Locate every leukocyte (white blood cell).
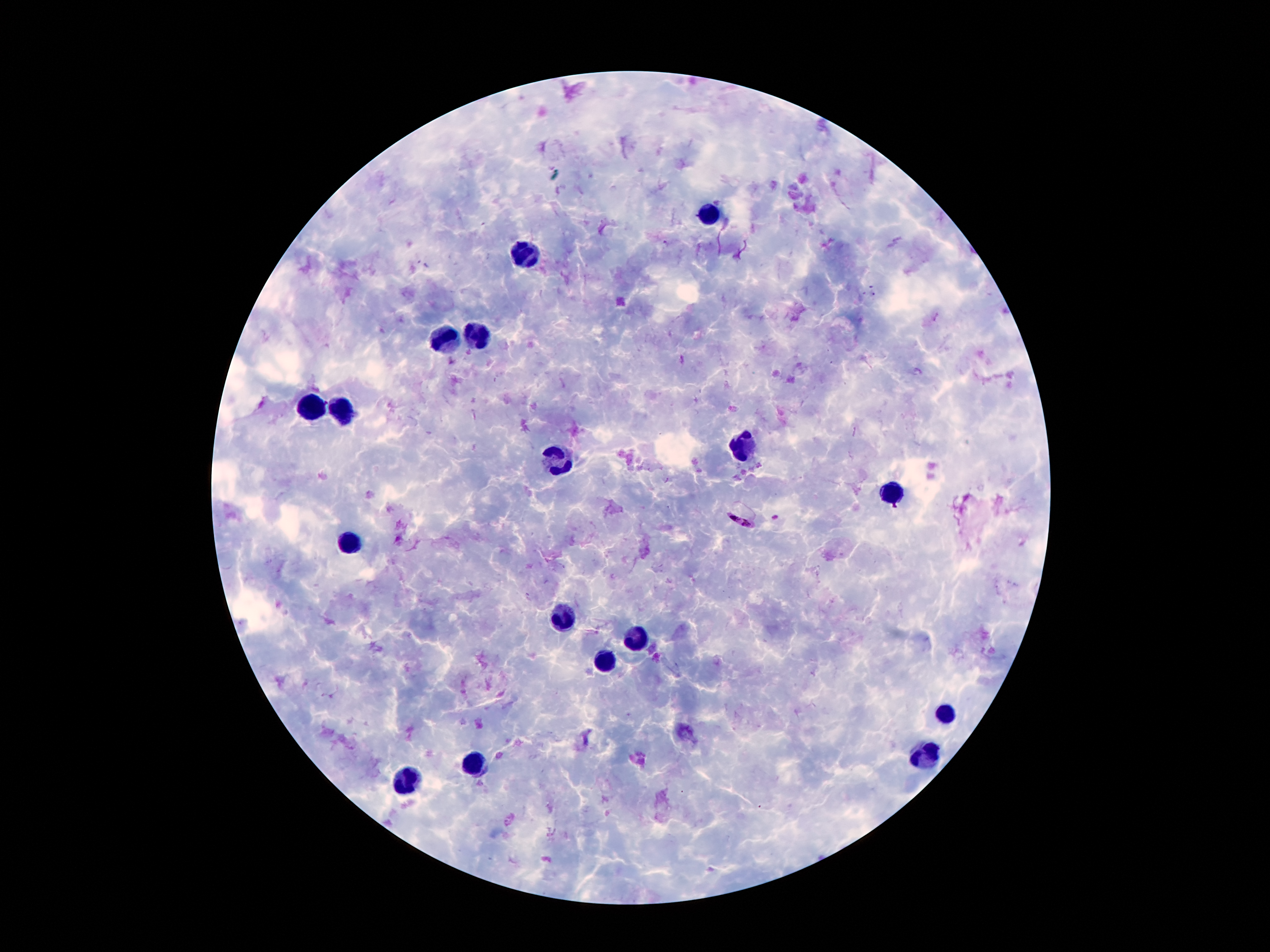
Approximate centers as [x, y] in pixels.
Leukocytes: [708, 209], [526, 254], [476, 334], [447, 336], [308, 406], [344, 409], [740, 443], [558, 463], [890, 490], [351, 542], [558, 617], [635, 640], [606, 661], [942, 715], [924, 758], [474, 765], [406, 779].

Plasmodium parasite locations: [778, 517], [740, 522]. Image is 1270×952 pixels. 100x magnification. Photographed through the microscope eyepiece with a smartphone camera. Patient malaria status: infected with Plasmodium falciparum. Single field of view. Giemsa-stained preparation. Thick blood smear.